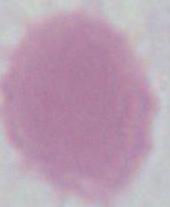
1000x magnification. An erythrocyte is shown. Photomicrograph.